Name the blood parasite species.
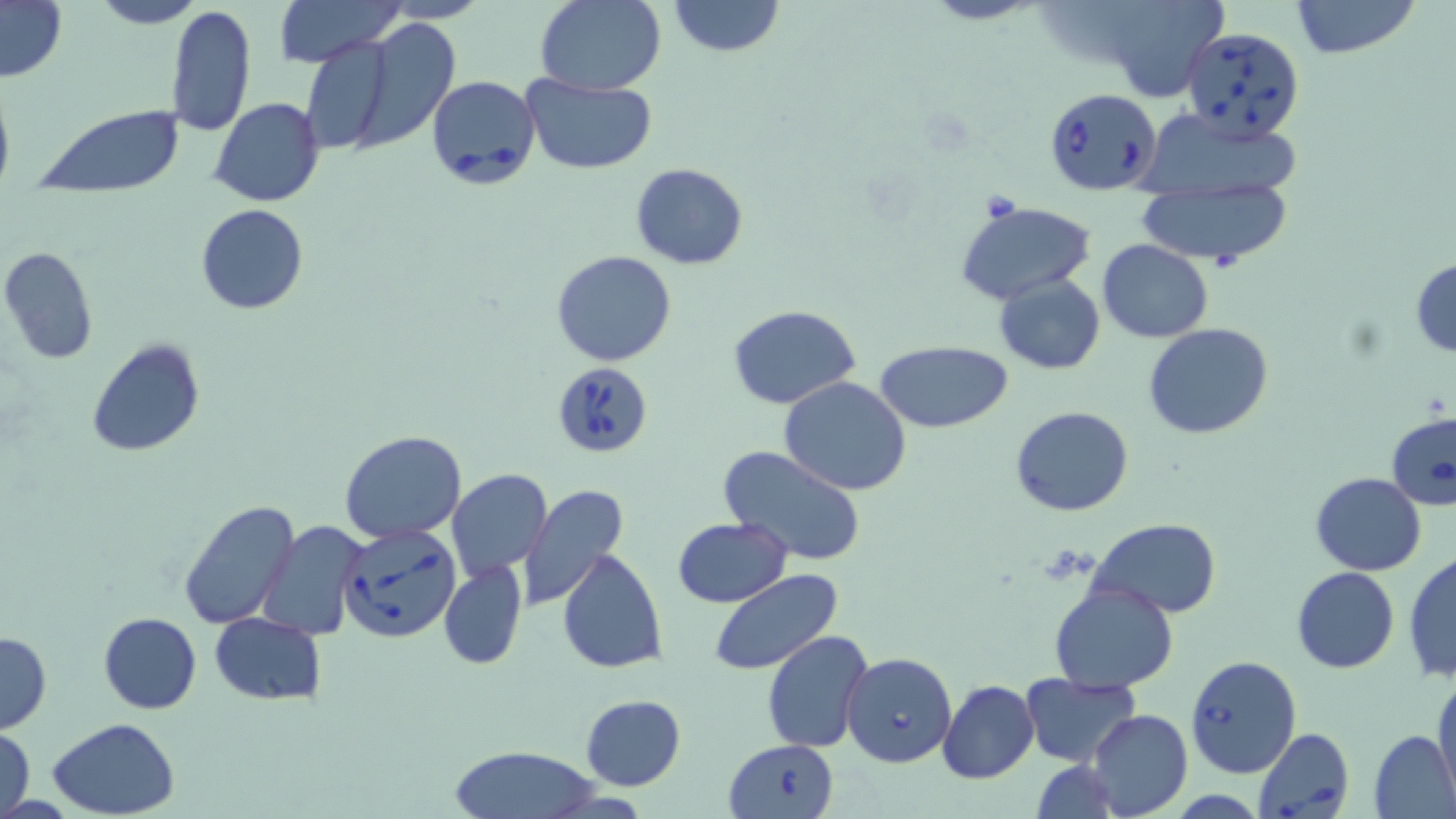
Babesia divergens.

Approximate bounding boxes as (x1,y1)-(x2,y2) corner pairs in pixels. Uninfected red blood cell locations: (90,0)-(202,27), (273,0)-(403,65), (535,0)-(665,95), (919,0)-(1046,25), (1095,0)-(1227,104), (1289,0)-(1421,59), (0,1)-(68,84), (668,1)-(783,55), (167,5)-(257,136), (352,18)-(459,148), (297,34)-(401,156), (521,75)-(657,176), (0,78)-(15,194), (209,97)-(325,206), (1135,105)-(1306,206), (32,106)-(185,195), (629,163)-(748,269), (1137,181)-(1293,267), (957,200)-(1095,302), (195,203)-(307,315), (1098,241)-(1213,342), (0,246)-(99,365), (552,250)-(676,366), (1410,259)-(1456,358), (995,275)-(1105,373), (727,304)-(861,410), (1141,322)-(1274,438), (86,337)-(204,457), (876,341)-(1012,433), (779,375)-(913,496), (1010,405)-(1134,516), (340,429)-(468,543), (718,446)-(867,566), (447,469)-(552,580), (1310,473)-(1427,576), (517,484)-(628,608), (178,497)-(302,631), (672,517)-(792,608), (1090,519)-(1222,617), (258,520)-(370,640), (557,546)-(666,675), (1404,552)-(1456,686), (439,559)-(528,670), (1291,567)-(1399,673), (710,571)-(843,674), (1049,581)-(1179,692), (98,611)-(201,712), (208,612)-(326,704), (761,630)-(873,754), (0,631)-(51,733), (1020,674)-(1141,768), (1432,676)-(1456,796), (937,680)-(1040,784), (579,694)-(686,791), (1085,708)-(1192,818), (48,718)-(183,817), (1,725)-(36,819), (1368,730)-(1456,819), (445,744)-(602,818), (1030,759)-(1120,819). Babesia divergens-infected red blood cell locations: (1181,28)-(1305,141), (426,73)-(541,191), (1043,87)-(1161,195), (553,361)-(654,458), (1385,411)-(1456,511), (337,523)-(460,643), (842,652)-(957,767), (1185,655)-(1303,778), (1251,728)-(1353,819), (723,739)-(839,819). Image is 1456×819 pixels. Light microscopy. Single field of view. Thin blood smear. May-Grünwald-Giemsa-stained preparation. 1000x magnification.